Report the malaria status of this cell.
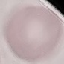
Uninfected.

Photographed with a smartphone camera at the microscope eyepiece. Thin blood smear. Cell patch, automatically extracted from a larger field of view and resized to 64 × 64 pixels. Giemsa-stained preparation.